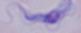

Summary:
  - Identification: trypanosome
  - Magnification: 1000x
  - Modality: micrograph